State which parasite is depicted.
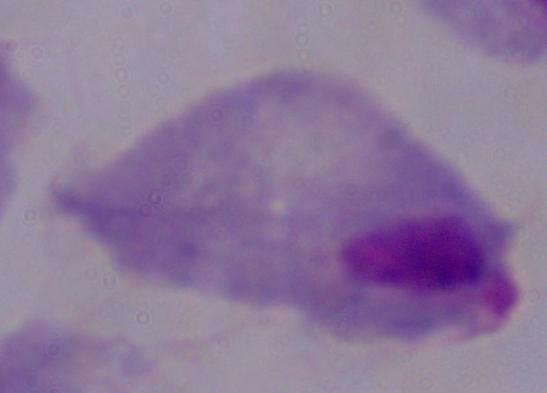

This is a trichomonad.

modality = photomicrograph
magnification = 1000x